Give the extent of all uninfected red blood cells.
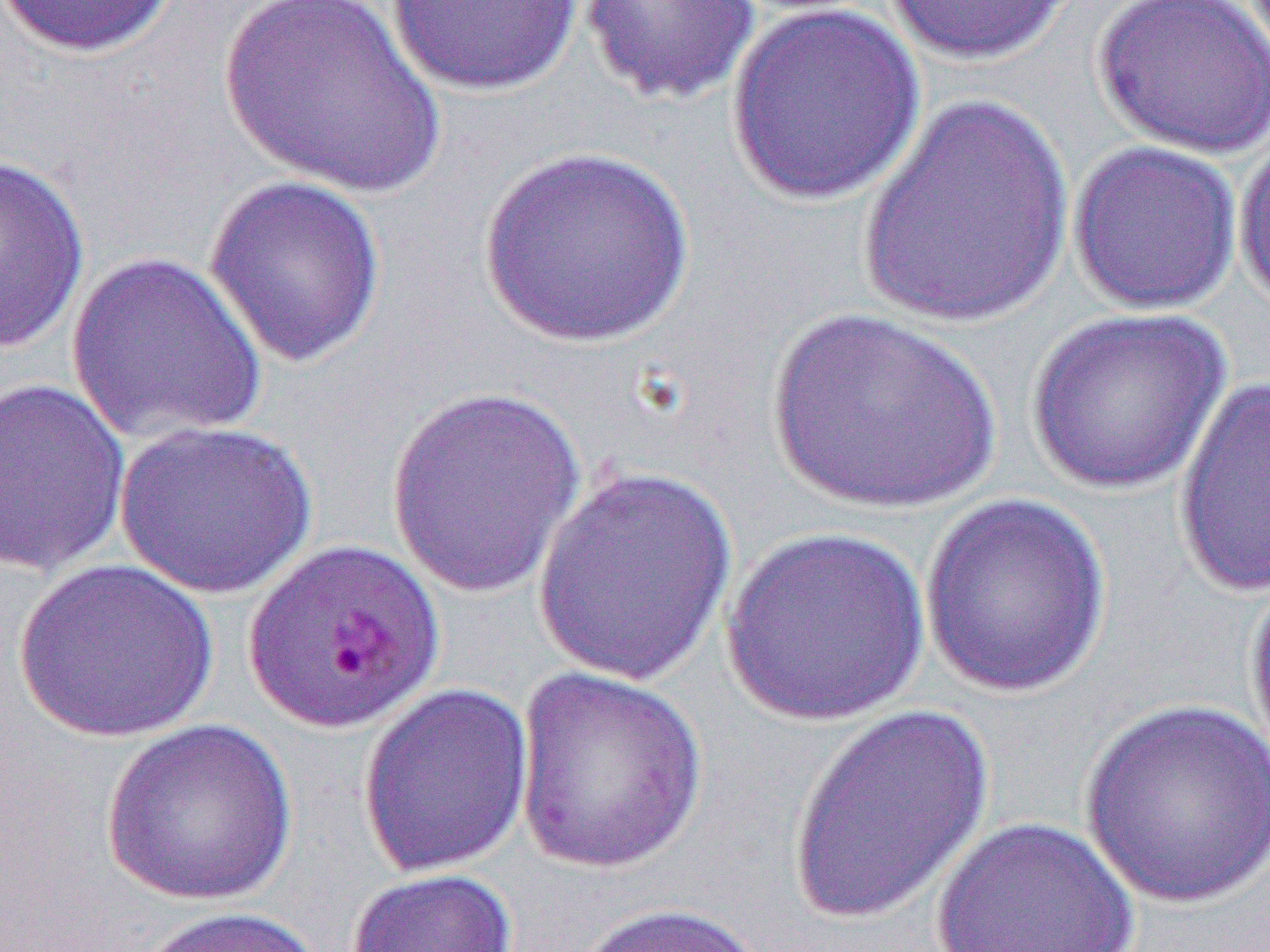

Approximate bounding boxes as (x1,y1)-(x2,y2) corner pairs in pixels.
Uninfected red blood cells: (0,0)-(179,59), (218,0)-(447,199), (579,0)-(763,107), (882,0)-(1078,66), (1091,0)-(1270,160), (383,1)-(586,96), (726,3)-(926,206), (858,92)-(1075,329), (1233,131)-(1270,311), (1067,141)-(1242,317), (477,147)-(696,349), (0,152)-(91,356), (203,174)-(387,370), (65,251)-(269,446), (1023,307)-(1233,496), (764,308)-(1004,516), (1173,375)-(1270,599), (0,376)-(132,577), (384,385)-(588,600), (114,419)-(318,601), (529,465)-(741,687), (917,493)-(1113,699), (720,527)-(933,727), (14,558)-(220,743), (1244,568)-(1270,773), (512,668)-(709,874), (357,682)-(535,880), (1078,699)-(1270,911), (785,703)-(999,927), (100,718)-(297,906), (929,816)-(1142,952), (345,868)-(520,952), (566,901)-(770,952), (132,905)-(330,952).

Slide-level diagnosis: Plasmodium falciparum. Image is 1270×952 pixels. Captured at 1000x magnification. Thin blood smear. One field of a larger specimen. Optical microscopy.